State which cell type is depicted.
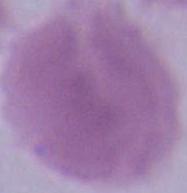
An erythrocyte.

1000x magnification. Photomicrograph.